Report the malaria status of this cell.
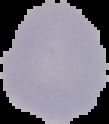
It is uninfected.

{
  "image_type": "segmented cell region on a black background",
  "preparation": "thin blood film",
  "image_size": "109×124 pixels"
}